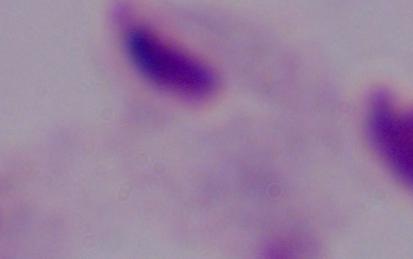

Summary:
  - Identification: trichomonad
  - Magnification: 1000x
  - Modality: photomicrograph